Evaluate for parasitized red blood cells.
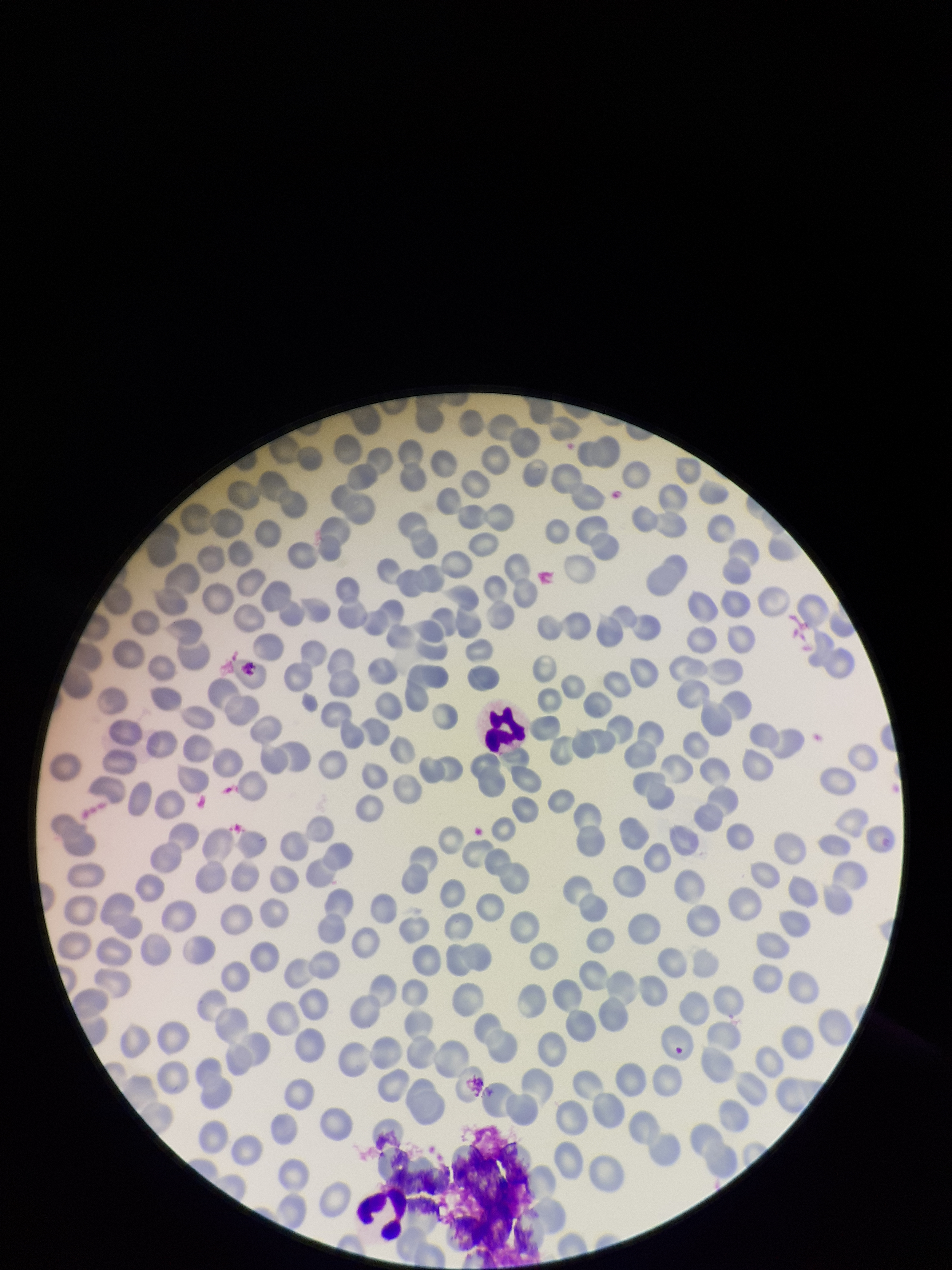
None identified.

red blood cell count = 260
image size = 952×1270 pixels
parasitized red blood cell count = 0
preparation = thin
field of view = single
capture = smartphone photograph through the microscope eyepiece
stain = Giemsa
patient malaria status = negative